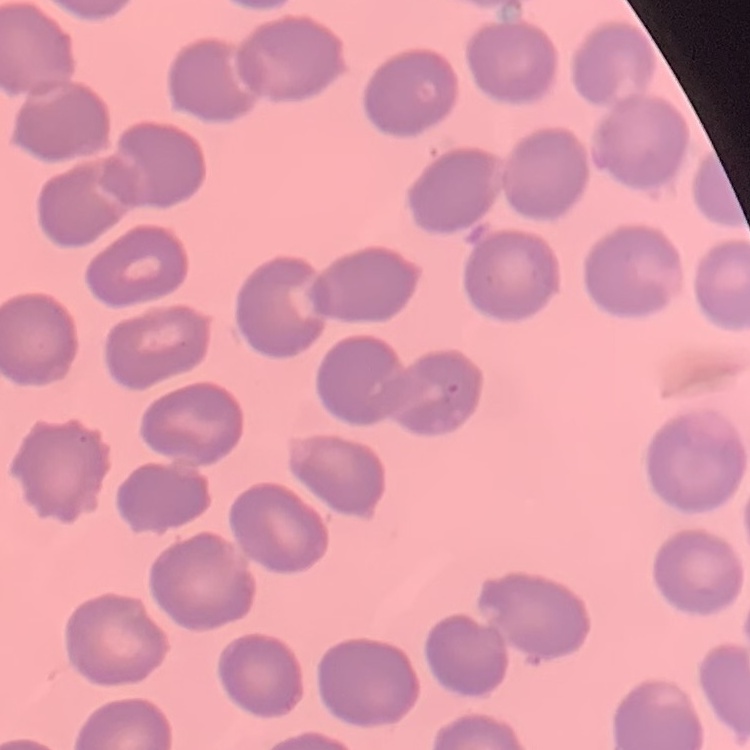
Summary:
  - Erythrocyte morphology: no rouleaux formation
  - Stain: Field's or Giemsa
  - Image type: square crop of a larger photomicrograph
  - Preparation: thin blood smear